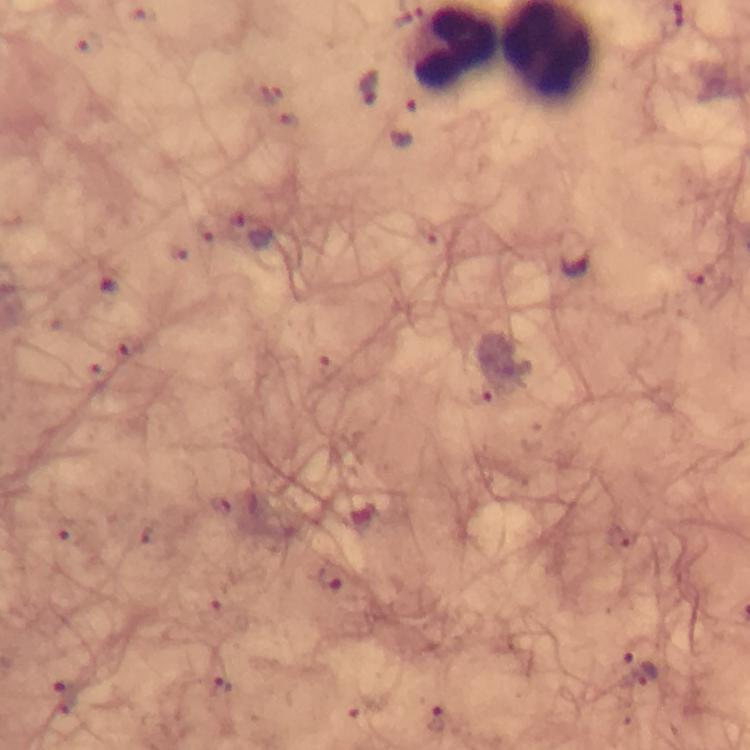
Approximate centers as [x, y] in pixels. Plasmodium parasite locations: [89, 42], [370, 88], [253, 233], [574, 254], [329, 578], [640, 668], [224, 686], [438, 716]. Giemsa-stained preparation. Photographed through the microscope with a smartphone camera. Thick smear. From a malaria diagnostic workup. 100x magnification. Immersion oil applied. A crop from one field of view. Image is 750×750 pixels.